Name the blood parasite species.
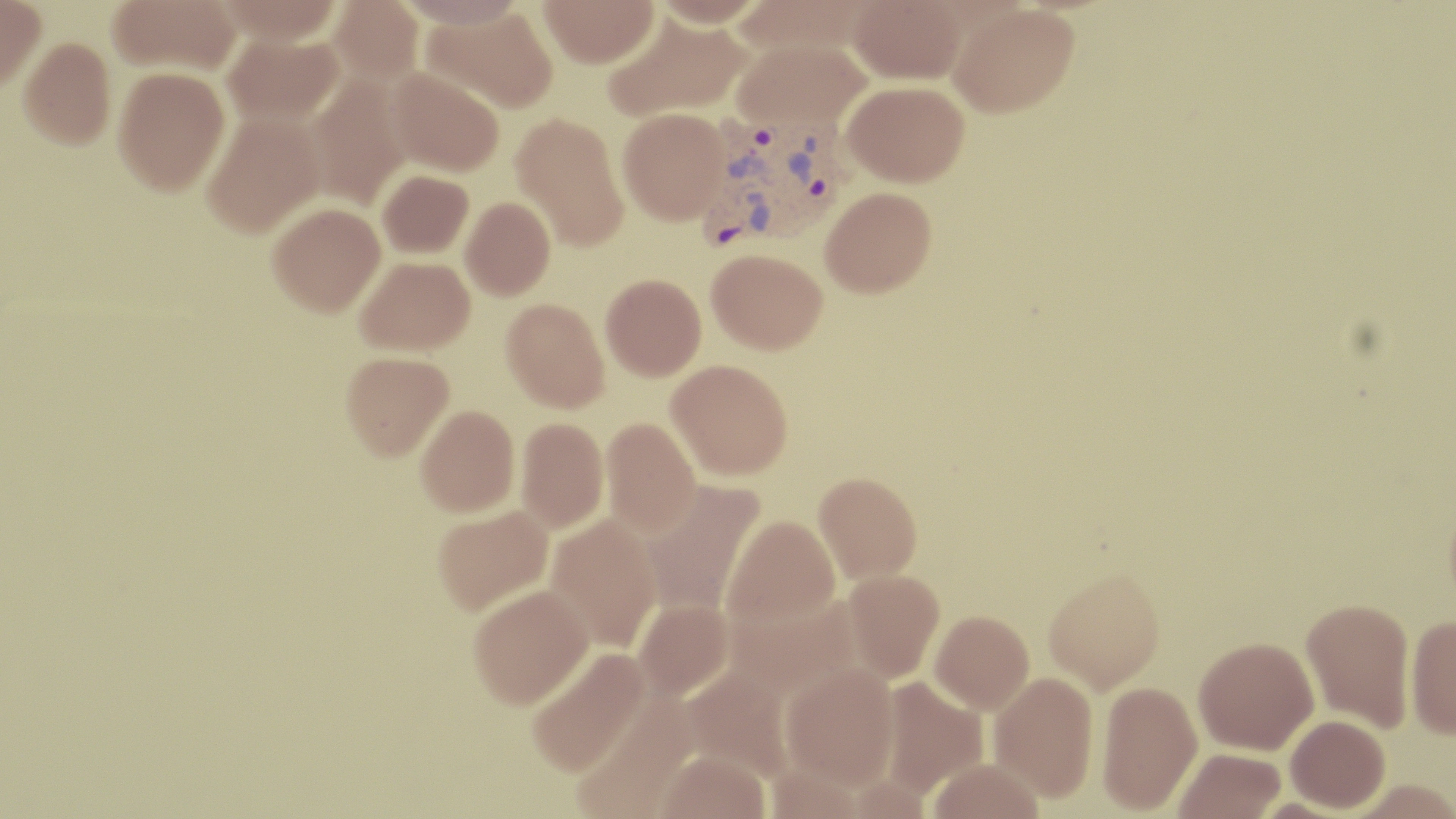
Plasmodium vivax.

Summary:
  - Coordinate format: approximate bounding boxes as named x1/y1/x2/y2 corners in pixels
  - Plasmodium vivax-infected red blood cell locations: (x1=701, y1=115, x2=850, y2=249)
  - Uninfected red blood cell locations: (x1=0, y1=0, x2=46, y2=91), (x1=108, y1=0, x2=241, y2=75), (x1=213, y1=0, x2=345, y2=43), (x1=327, y1=0, x2=425, y2=85), (x1=394, y1=0, x2=526, y2=28), (x1=539, y1=0, x2=659, y2=67), (x1=649, y1=0, x2=769, y2=27), (x1=731, y1=0, x2=878, y2=57), (x1=848, y1=0, x2=965, y2=84), (x1=947, y1=2, x2=1080, y2=118), (x1=422, y1=7, x2=558, y2=114), (x1=603, y1=11, x2=751, y2=122), (x1=223, y1=32, x2=345, y2=127), (x1=18, y1=36, x2=116, y2=149), (x1=733, y1=39, x2=870, y2=131), (x1=113, y1=66, x2=230, y2=195), (x1=388, y1=68, x2=505, y2=177), (x1=305, y1=73, x2=411, y2=210), (x1=843, y1=81, x2=969, y2=187), (x1=618, y1=107, x2=730, y2=225), (x1=201, y1=111, x2=326, y2=237), (x1=511, y1=113, x2=630, y2=252), (x1=377, y1=170, x2=474, y2=258), (x1=820, y1=186, x2=936, y2=297), (x1=460, y1=197, x2=555, y2=300), (x1=267, y1=202, x2=385, y2=316), (x1=707, y1=249, x2=827, y2=353), (x1=355, y1=256, x2=475, y2=356), (x1=601, y1=273, x2=707, y2=379), (x1=501, y1=298, x2=610, y2=412), (x1=340, y1=351, x2=454, y2=460), (x1=667, y1=359, x2=793, y2=480), (x1=416, y1=405, x2=520, y2=516), (x1=601, y1=416, x2=701, y2=537), (x1=515, y1=417, x2=609, y2=533), (x1=814, y1=471, x2=923, y2=583), (x1=641, y1=480, x2=764, y2=617), (x1=432, y1=505, x2=553, y2=616), (x1=547, y1=515, x2=662, y2=653), (x1=722, y1=515, x2=840, y2=632), (x1=1043, y1=567, x2=1167, y2=691), (x1=843, y1=569, x2=945, y2=683), (x1=468, y1=583, x2=594, y2=708), (x1=725, y1=593, x2=861, y2=701), (x1=1301, y1=597, x2=1415, y2=732), (x1=634, y1=599, x2=733, y2=701), (x1=930, y1=610, x2=1034, y2=713), (x1=1406, y1=615, x2=1456, y2=738), (x1=1194, y1=636, x2=1318, y2=754), (x1=525, y1=648, x2=650, y2=777), (x1=780, y1=663, x2=899, y2=788), (x1=680, y1=665, x2=797, y2=780), (x1=988, y1=672, x2=1099, y2=801), (x1=879, y1=677, x2=988, y2=797), (x1=1096, y1=680, x2=1202, y2=815), (x1=571, y1=695, x2=698, y2=819), (x1=1285, y1=714, x2=1390, y2=812), (x1=1174, y1=748, x2=1286, y2=819), (x1=656, y1=749, x2=771, y2=819), (x1=927, y1=758, x2=1046, y2=819), (x1=1347, y1=779, x2=1456, y2=819)
  - Preparation: thin blood smear
  - Magnification: 1000x
  - Modality: optical microscopy
  - Field of view: single
  - Stain: May-Grünwald-Giemsa
  - Image size: 1456×819 pixels